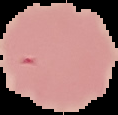

Summary:
  - Malaria status: uninfected
  - Image type: segmented cell region on a black background
  - Preparation: thin blood film
  - Image size: 118×115 pixels